Classify this cell by malaria status.
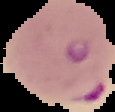

Parasitized.

preparation: thin blood film
image_size: 115×112 pixels
image_type: segmented cell region with the area outside set to black